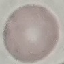

result: no malaria parasites detected
capture: smartphone through the microscope eyepiece
preparation: thin blood film
stain: Giemsa
image_type: cell patch, automatically extracted from a larger field of view and resized to 64 × 64 pixels